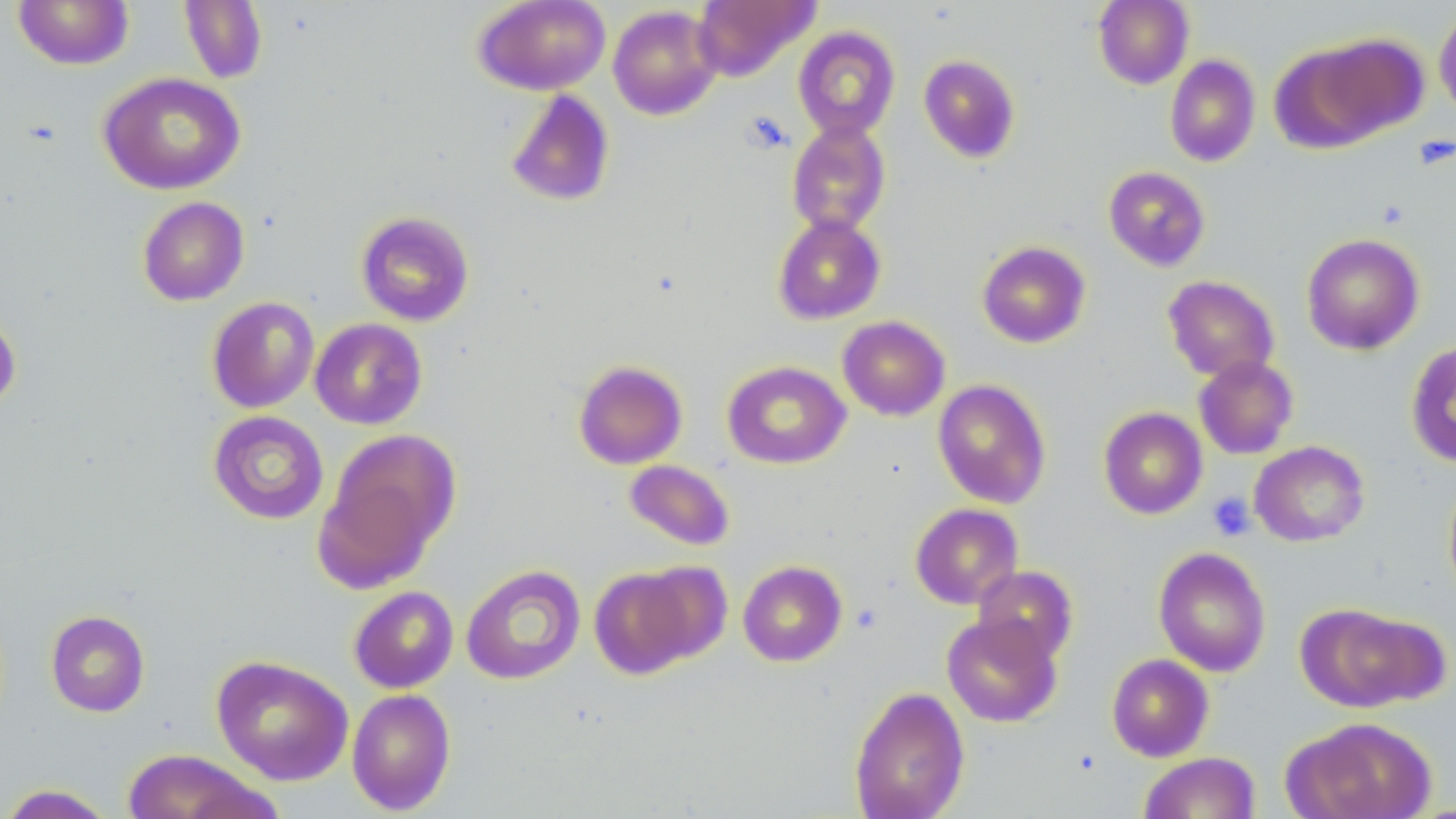
Approximate bounding boxes as (x1, y1, x2, y2) in pixels. Uninfected red blood cell locations: (12, 0, 135, 70), (179, 0, 268, 83), (473, 0, 610, 95), (692, 0, 819, 81), (1092, 0, 1194, 89), (607, 4, 723, 120), (1434, 9, 1456, 119), (792, 26, 901, 141), (1313, 32, 1430, 140), (1269, 43, 1389, 154), (918, 54, 1021, 163), (1165, 54, 1260, 167), (97, 71, 246, 195), (504, 90, 616, 207), (786, 120, 891, 236), (1103, 166, 1211, 271), (137, 196, 249, 306), (355, 210, 475, 326), (772, 214, 887, 325), (1301, 232, 1425, 355), (976, 240, 1091, 348), (1163, 275, 1279, 382), (206, 296, 320, 413), (0, 309, 22, 413), (837, 315, 950, 421), (309, 318, 428, 430), (1406, 341, 1456, 467), (1193, 356, 1299, 459), (573, 360, 688, 469), (722, 361, 851, 469), (932, 378, 1052, 509), (1098, 407, 1208, 520), (208, 410, 329, 524), (325, 429, 461, 560), (1249, 441, 1369, 547), (624, 459, 735, 551), (312, 473, 437, 594), (1443, 474, 1456, 601), (910, 503, 1023, 609), (1153, 546, 1271, 677), (737, 560, 848, 667), (635, 561, 733, 663), (461, 564, 585, 685), (589, 565, 700, 679), (972, 565, 1078, 664), (349, 586, 458, 693), (1298, 602, 1435, 712), (45, 610, 150, 717), (942, 613, 1062, 727), (1106, 653, 1214, 762), (211, 655, 353, 786), (848, 685, 970, 819), (346, 688, 456, 814), (1289, 716, 1436, 819), (123, 749, 270, 819), (1139, 752, 1260, 819), (0, 784, 117, 818). Platelet locations: (742, 112, 791, 153), (1414, 136, 1453, 170), (1207, 492, 1255, 540), (851, 603, 883, 632). Slide-level diagnosis: negative for blood parasites. Optical microscopy. 1000x magnification. Image is 1456×819 pixels. Single field of view. Thin blood film. May-Grünwald-Giemsa stain.